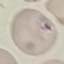
Summary:
  - Malaria status: uninfected
  - Preparation: thin blood smear
  - Stain: Giemsa
  - Image type: cell patch, automatically extracted from a larger field of view and resized to 64 × 64 pixels
  - Capture: smartphone through the microscope eyepiece